Report the malaria status of this cell.
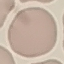

It is uninfected.

{
  "image_type": "cell patch, automatically extracted from a larger field of view and resized to 64 × 64 pixels",
  "stain": "Giemsa",
  "capture": "smartphone through the microscope eyepiece",
  "preparation": "thin blood film"
}